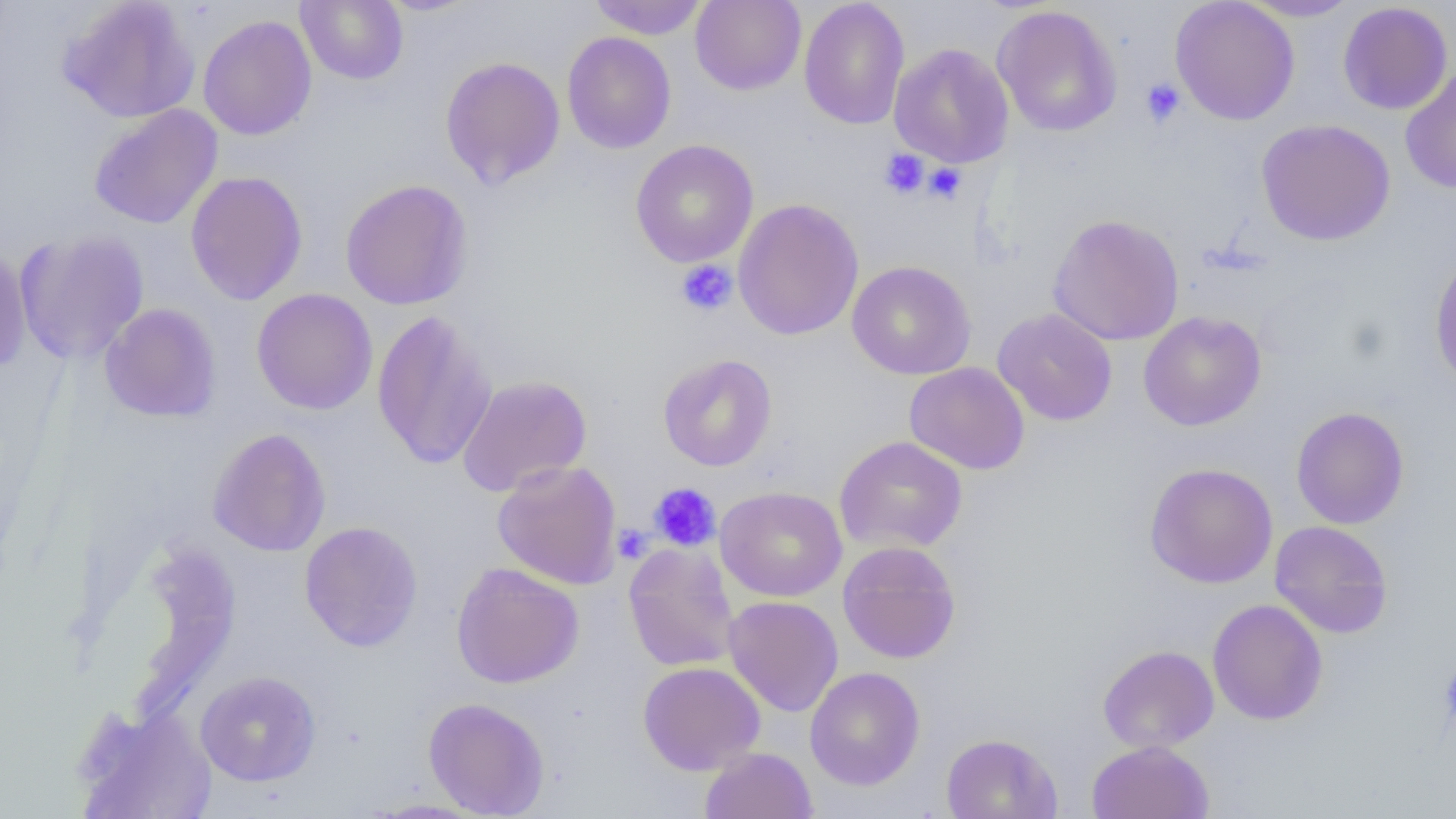
Summary:
  - Coordinate format: approximate bounding boxes as (x1,y1)-(x2,y2) corner pairs in pixels
  - Uninfected red blood cell locations: (59,0)-(200,124), (296,0)-(409,85), (376,0)-(483,16), (589,0)-(708,39), (690,0)-(806,95), (799,0)-(910,130), (1170,0)-(1300,125), (1239,0)-(1360,22), (1337,2)-(1453,115), (992,5)-(1123,138), (197,15)-(317,141), (561,31)-(676,153), (889,43)-(1014,167), (439,56)-(566,189), (1399,64)-(1456,194), (88,104)-(223,229), (1256,119)-(1395,246), (630,139)-(759,267), (185,171)-(308,305), (340,179)-(474,311), (733,198)-(864,340), (1048,213)-(1185,346), (14,229)-(150,365), (0,242)-(31,373), (1429,251)-(1456,389), (847,260)-(976,379), (251,288)-(378,415), (99,303)-(222,423), (993,308)-(1118,426), (372,309)-(497,470), (1138,311)-(1267,432), (658,353)-(777,471), (904,362)-(1030,475), (456,375)-(592,497), (1291,406)-(1409,529), (208,427)-(331,557), (834,435)-(968,554), (492,460)-(623,589), (1144,462)-(1278,588), (715,486)-(847,602), (1269,520)-(1393,639), (299,521)-(423,652), (623,540)-(740,672), (837,540)-(962,664), (451,562)-(584,689), (723,595)-(844,717), (1207,599)-(1328,725), (1098,645)-(1219,753), (638,661)-(766,774), (805,667)-(925,791), (195,670)-(321,786), (423,697)-(550,817), (72,703)-(218,819), (941,732)-(1062,819), (1086,740)-(1214,819), (700,747)-(817,819), (365,799)-(487,818)
  - Platelet locations: (1140,77)-(1186,127), (880,149)-(929,199), (924,162)-(967,205), (676,259)-(738,317), (648,482)-(721,552), (613,524)-(653,565), (1438,653)-(1456,739)
  - Slide-level diagnosis: no evidence of blood parasites
  - Field of view: one of a larger specimen
  - Magnification: 1000x
  - Modality: optical microscopy
  - Preparation: thin blood smear
  - Image size: 1456×819 pixels